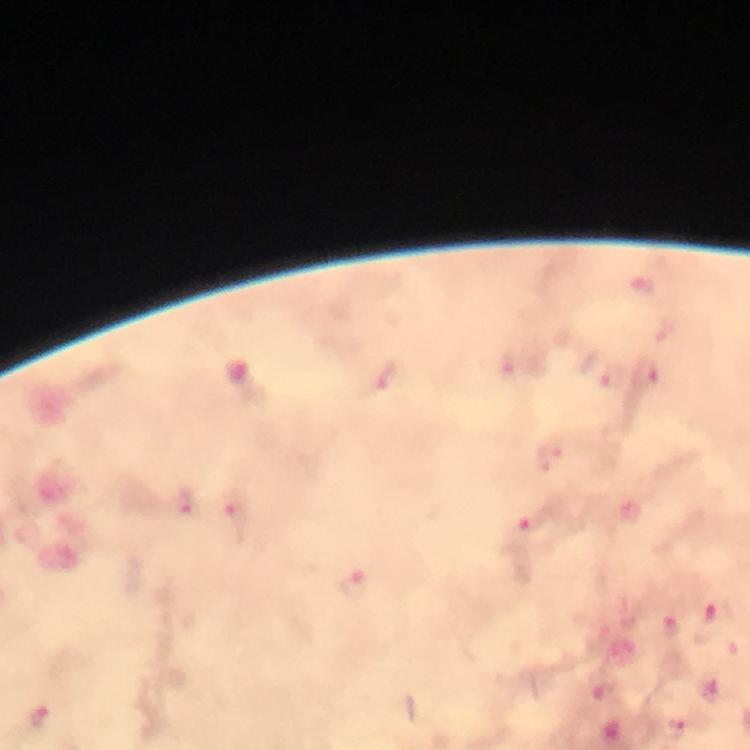

context = from a diagnostic examination for malaria
Plasmodium parasite locations = approximate centers as [x, y] in pixels: [645, 287], [511, 368], [601, 373], [646, 373], [385, 377], [185, 503], [236, 512], [528, 524], [356, 584], [713, 624], [673, 625], [39, 717], [675, 727]
capture = smartphone mounted on the microscope
image size = 750×750 pixels
cropped from = one field of view
magnification = 100x
stain = Giemsa
immersion oil = applied
preparation = thick smear